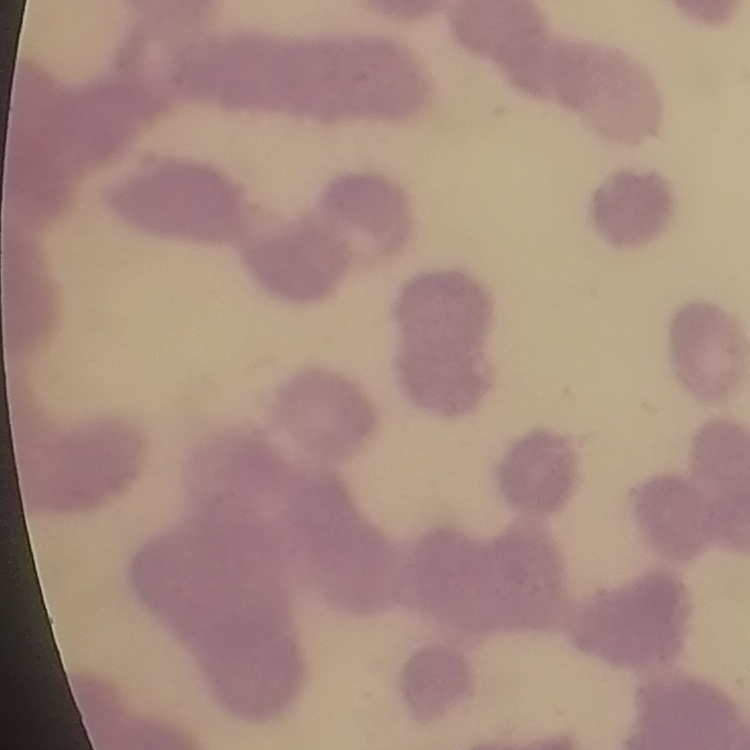
red blood cell morphology = rouleaux formation
stain = Field's or Giemsa
image type = square crop of a larger photomicrograph
preparation = thin blood film